Classify this cell by malaria status.
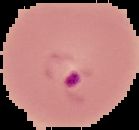
Parasitized.

{
  "preparation": "thin blood film",
  "image_size": "139×130 pixels",
  "image_type": "cell region segmented out of the field of view; surrounding area masked to black"
}